Identify the cell.
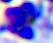

This is a leukocyte.

Photomicrograph. 400x magnification.